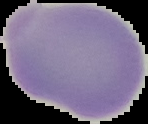

Summary:
  - Preparation: thin blood film
  - Image size: 148×124 pixels
  - Image type: segmented cell region with the area outside set to black
  - Result: no Plasmodium parasites detected